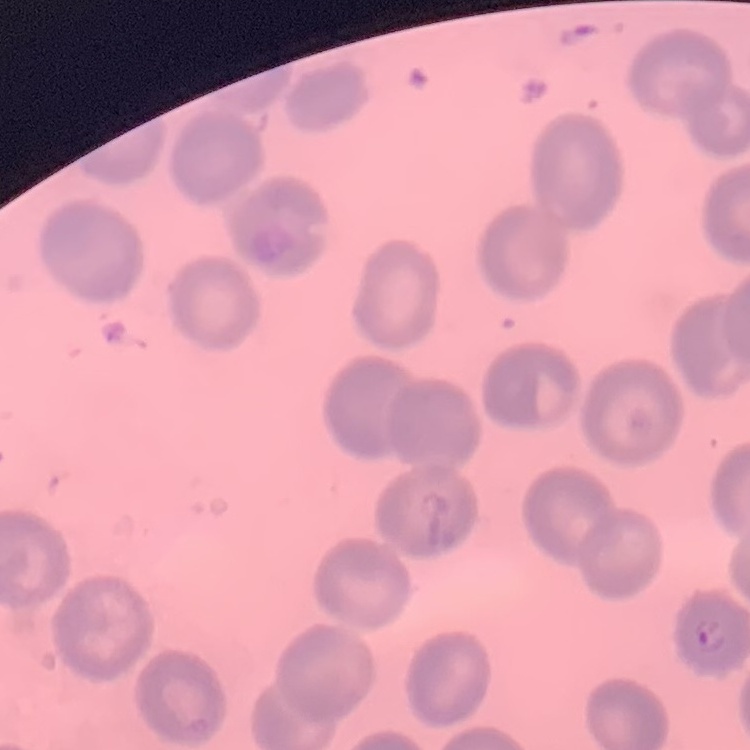
Summary:
  - Red blood cell morphology: no rouleaux formation
  - Image type: square crop of a larger photomicrograph
  - Preparation: thin peripheral smear
  - Stain: Field's or Giemsa